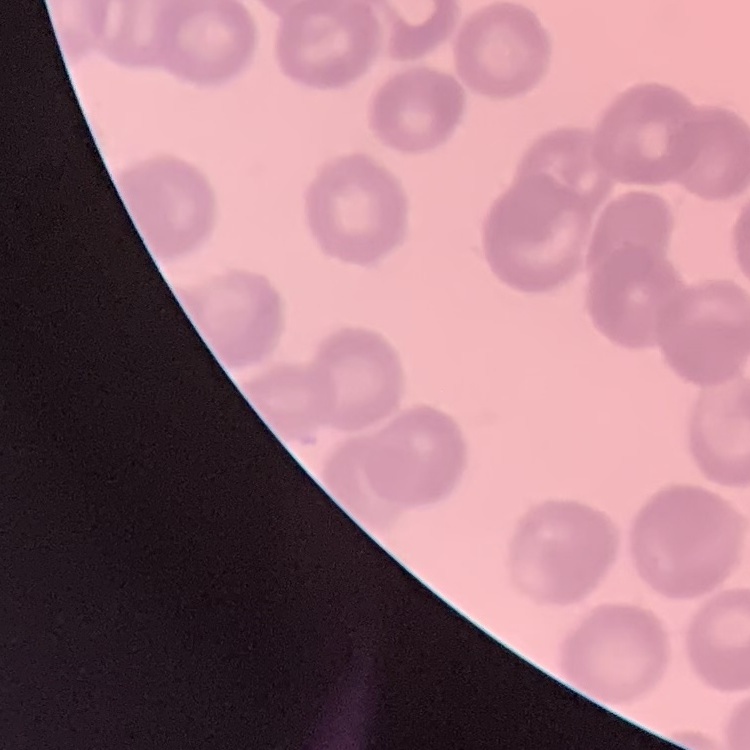

Summary:
  - Red blood cell morphology: rouleaux formation
  - Image type: square crop of a larger photomicrograph
  - Stain: Field's or Giemsa
  - Preparation: thin blood film